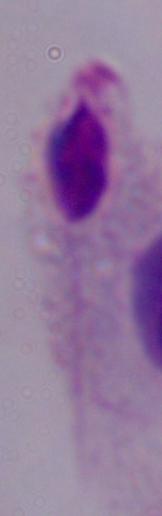
modality = photomicrograph
identification = trichomonad
magnification = 1000x